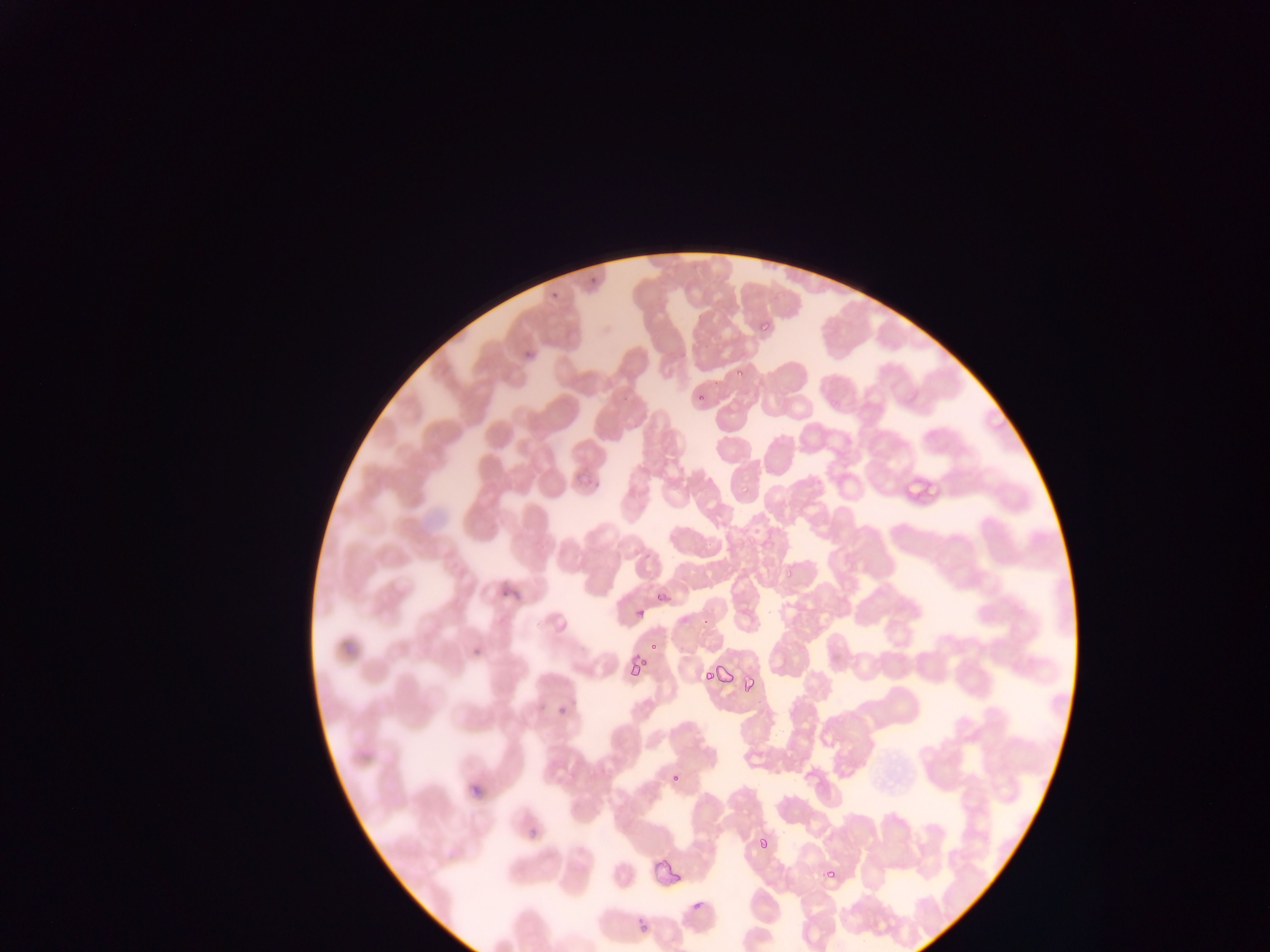
Approximate bounding boxes as [left, top, right, bottom] in pixels.
Summary:
  - Malaria parasite locations: [758, 324, 775, 335], [694, 395, 704, 402], [782, 556, 802, 581], [656, 590, 669, 602], [636, 596, 643, 620], [650, 641, 664, 655], [627, 661, 643, 680], [703, 666, 715, 681], [719, 666, 738, 686], [741, 674, 758, 695], [553, 703, 567, 717], [668, 770, 686, 789], [760, 835, 770, 849], [823, 873, 835, 880], [637, 927, 649, 935] | approximate [x, y] pixel centers of objects too small to bound: [739, 376]
  - Capture: mobile-phone photograph through a microscope
  - Image size: 1270×952 pixels
  - Preparation: thin blood film
  - Country: Ghana
  - Field of view: single